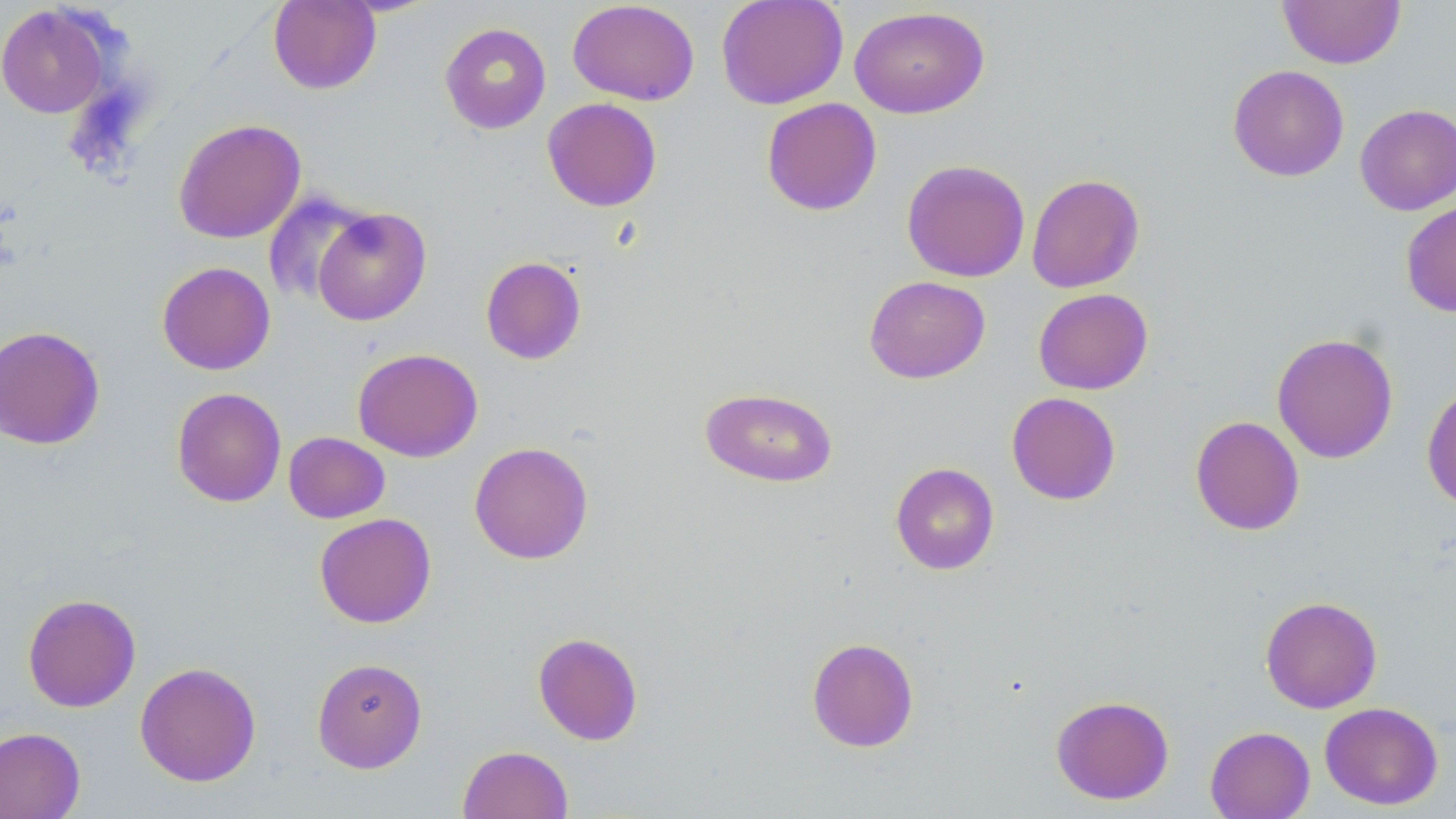
slide_level_diagnosis: negative for blood parasites
modality: light microscopy
uninfected_red_blood_cell_locations: 'approximate bounding boxes as named x1/y1/x2/y2 corners in pixels: (x1=268, y1=0, x2=381, y2=94), (x1=568, y1=0, x2=700, y2=105), (x1=716, y1=0, x2=848, y2=109), (x1=1278, y1=0, x2=1406, y2=69), (x1=0, y1=4, x2=110, y2=118), (x1=849, y1=6, x2=990, y2=118), (x1=439, y1=22, x2=551, y2=134), (x1=1227, y1=64, x2=1349, y2=181), (x1=542, y1=97, x2=662, y2=212), (x1=761, y1=97, x2=883, y2=216), (x1=1355, y1=103, x2=1456, y2=215), (x1=173, y1=118, x2=306, y2=244), (x1=901, y1=159, x2=1030, y2=282), (x1=1026, y1=173, x2=1145, y2=293), (x1=262, y1=190, x2=374, y2=308), (x1=1401, y1=201, x2=1456, y2=317), (x1=312, y1=206, x2=431, y2=326), (x1=480, y1=256, x2=587, y2=365), (x1=157, y1=261, x2=275, y2=375), (x1=864, y1=275, x2=990, y2=383), (x1=1033, y1=288, x2=1153, y2=395), (x1=0, y1=325, x2=105, y2=450), (x1=1271, y1=332, x2=1399, y2=464), (x1=352, y1=347, x2=483, y2=462), (x1=1421, y1=381, x2=1456, y2=511), (x1=171, y1=387, x2=287, y2=507), (x1=700, y1=387, x2=838, y2=488), (x1=1006, y1=392, x2=1122, y2=505), (x1=1190, y1=415, x2=1305, y2=536), (x1=283, y1=431, x2=390, y2=523), (x1=469, y1=441, x2=594, y2=564), (x1=890, y1=462, x2=1000, y2=575), (x1=314, y1=512, x2=437, y2=628), (x1=22, y1=593, x2=141, y2=713), (x1=1260, y1=595, x2=1383, y2=713), (x1=533, y1=631, x2=643, y2=745), (x1=806, y1=637, x2=919, y2=753), (x1=311, y1=657, x2=428, y2=773), (x1=134, y1=661, x2=261, y2=787), (x1=1051, y1=695, x2=1175, y2=805), (x1=1319, y1=702, x2=1444, y2=810), (x1=1204, y1=725, x2=1315, y2=819), (x1=0, y1=726, x2=85, y2=818), (x1=457, y1=744, x2=574, y2=819)'
field_of_view: single
preparation: thin blood smear
stain: May-Grünwald-Giemsa
magnification: 1000x
image_size: 1456×819 pixels